Locate and identify every blood parasite.
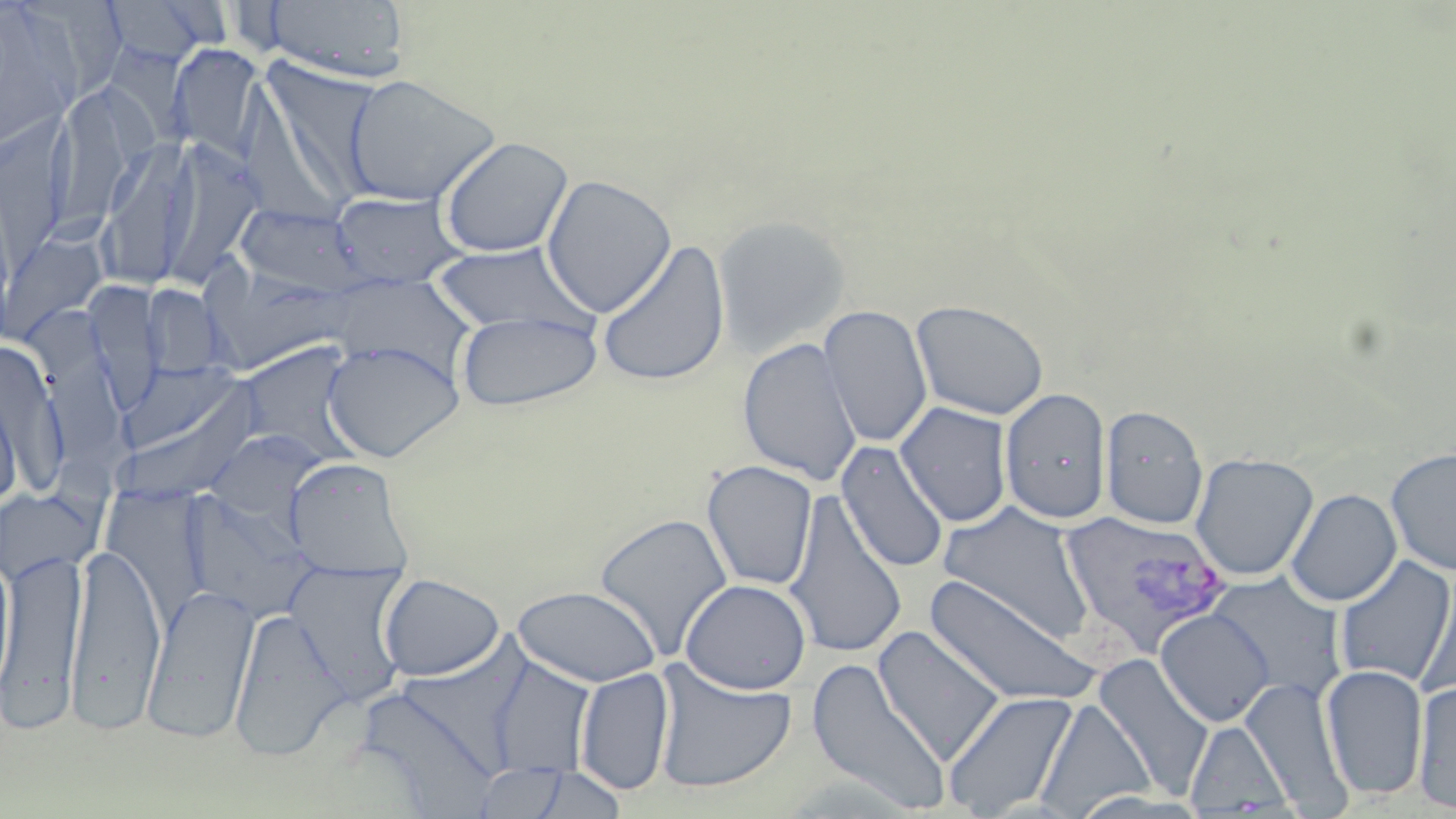

Approximate bounding boxes as named x1/y1/x2/y2 corners in pixels.
Plasmodium vivax-infected red blood cells: (x1=1059, y1=510, x2=1232, y2=658).
No Plasmodium falciparum, Plasmodium ovale, Plasmodium malariae, Babesia divergens, or Trypanosoma brucei observed.

{
  "slide_level_diagnosis": "Plasmodium vivax",
  "modality": "optical microscopy",
  "preparation": "thin blood smear",
  "image_size": "1456×819 pixels",
  "field_of_view": "one of a larger specimen",
  "uninfected_red_blood_cell_locations": "approximate bounding boxes as named x1/y1/x2/y2 corners in pixels: (x1=0, y1=0, x2=83, y2=153), (x1=101, y1=0, x2=222, y2=69), (x1=261, y1=0, x2=411, y2=84), (x1=167, y1=44, x2=267, y2=161), (x1=253, y1=54, x2=384, y2=206), (x1=341, y1=74, x2=500, y2=207), (x1=46, y1=85, x2=148, y2=238), (x1=0, y1=109, x2=75, y2=260), (x1=438, y1=136, x2=574, y2=258), (x1=98, y1=137, x2=199, y2=291), (x1=156, y1=137, x2=264, y2=291), (x1=541, y1=174, x2=677, y2=318), (x1=329, y1=191, x2=467, y2=290), (x1=233, y1=203, x2=371, y2=299), (x1=712, y1=214, x2=850, y2=358), (x1=596, y1=239, x2=731, y2=387), (x1=432, y1=243, x2=595, y2=338), (x1=201, y1=264, x2=352, y2=374), (x1=82, y1=281, x2=164, y2=411), (x1=142, y1=284, x2=230, y2=379), (x1=911, y1=298, x2=1049, y2=420), (x1=819, y1=304, x2=933, y2=448), (x1=456, y1=310, x2=603, y2=411), (x1=737, y1=337, x2=862, y2=486), (x1=322, y1=340, x2=464, y2=463), (x1=1, y1=342, x2=67, y2=497), (x1=232, y1=343, x2=363, y2=462), (x1=112, y1=366, x2=263, y2=506), (x1=999, y1=386, x2=1111, y2=525), (x1=0, y1=391, x2=21, y2=512), (x1=895, y1=402, x2=1013, y2=527), (x1=1100, y1=404, x2=1208, y2=529), (x1=204, y1=430, x2=324, y2=525), (x1=836, y1=441, x2=950, y2=574), (x1=1385, y1=446, x2=1456, y2=577), (x1=1190, y1=453, x2=1318, y2=581), (x1=286, y1=458, x2=414, y2=578), (x1=701, y1=459, x2=818, y2=591), (x1=0, y1=488, x2=97, y2=585), (x1=1285, y1=488, x2=1402, y2=606), (x1=181, y1=489, x2=315, y2=623), (x1=784, y1=492, x2=908, y2=659), (x1=936, y1=502, x2=1096, y2=643), (x1=594, y1=512, x2=734, y2=662), (x1=66, y1=542, x2=166, y2=731), (x1=1, y1=545, x2=89, y2=731), (x1=0, y1=551, x2=17, y2=699), (x1=1334, y1=556, x2=1455, y2=689), (x1=285, y1=561, x2=411, y2=702), (x1=1416, y1=571, x2=1456, y2=700), (x1=1205, y1=572, x2=1347, y2=706), (x1=379, y1=574, x2=505, y2=682), (x1=923, y1=576, x2=1102, y2=707), (x1=680, y1=578, x2=812, y2=694), (x1=142, y1=583, x2=260, y2=744), (x1=512, y1=586, x2=662, y2=687), (x1=228, y1=607, x2=346, y2=760), (x1=1155, y1=608, x2=1275, y2=726), (x1=873, y1=626, x2=1006, y2=767), (x1=485, y1=655, x2=596, y2=777), (x1=1092, y1=655, x2=1213, y2=797), (x1=806, y1=657, x2=952, y2=815), (x1=650, y1=660, x2=797, y2=795), (x1=1320, y1=664, x2=1429, y2=800), (x1=575, y1=667, x2=674, y2=796), (x1=1240, y1=676, x2=1352, y2=812), (x1=1412, y1=680, x2=1456, y2=814), (x1=943, y1=690, x2=1079, y2=818), (x1=1035, y1=698, x2=1155, y2=817), (x1=1184, y1=718, x2=1295, y2=816), (x1=472, y1=760, x2=628, y2=819)",
  "magnification": "1000x",
  "stain": "May-Grünwald-Giemsa"
}